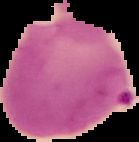
Image is 139×142 pixels. Result: Plasmodium parasites detected. Cell region segmented out of the field of view; the surrounding area is masked to black. From a thin blood smear.